Classify this cell by malaria status.
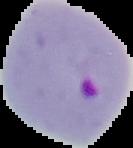
Parasitized.

Summary:
  - Image type: cell region segmented out of the field of view; surrounding area masked to black
  - Image size: 133×148 pixels
  - Preparation: thin blood smear